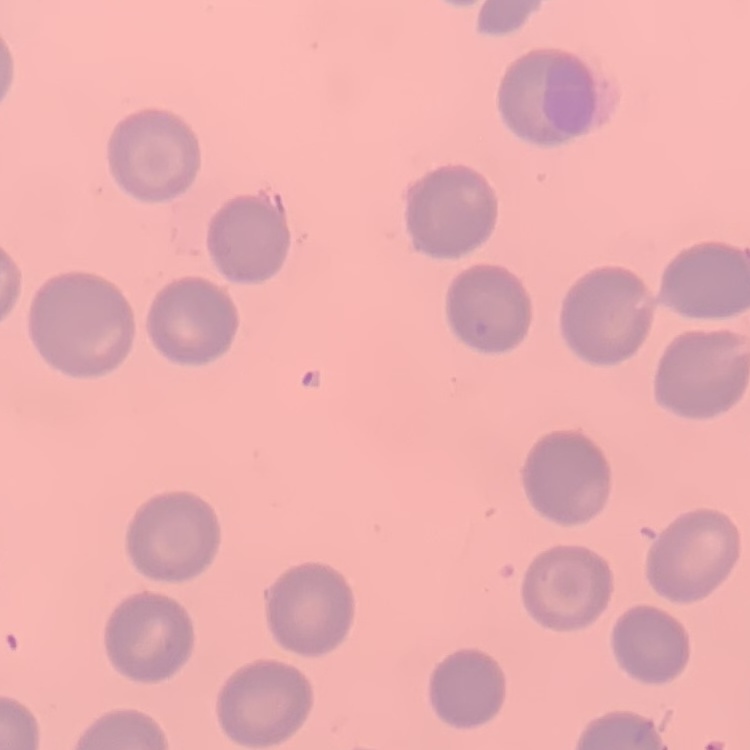

Summary:
  - Erythrocyte morphology: no rouleaux formation
  - Image type: square crop of a larger photomicrograph
  - Preparation: thin blood film
  - Stain: Field's or Giemsa